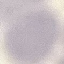
Summary:
  - Malaria status: uninfected
  - Image type: cell patch, automatically extracted from a larger field of view and resized to 64 × 64 pixels
  - Preparation: thin blood film
  - Stain: Giemsa
  - Capture: smartphone camera at the microscope eyepiece